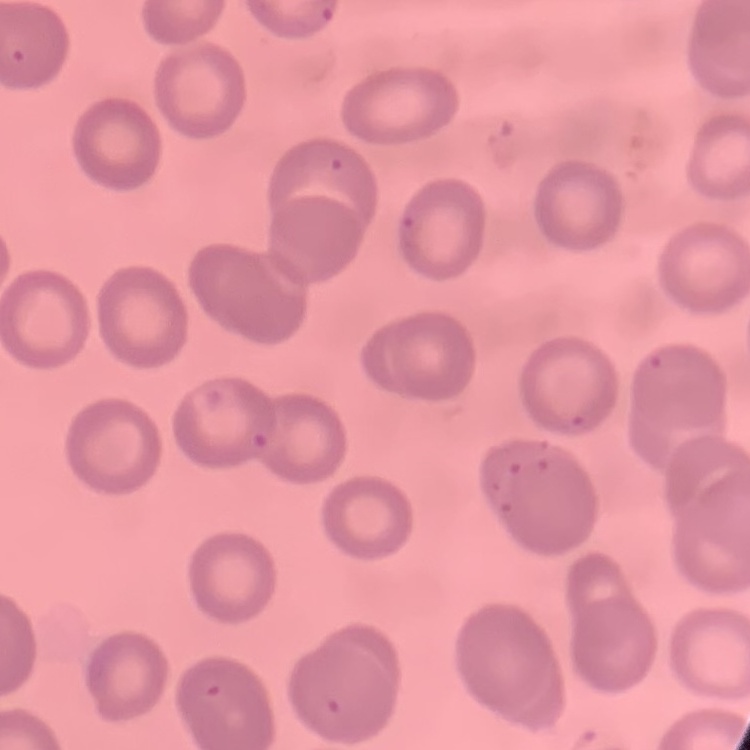

red blood cell morphology = no rouleaux formation
stain = Field's or Giemsa
preparation = thin peripheral smear
image type = square crop of a larger photomicrograph